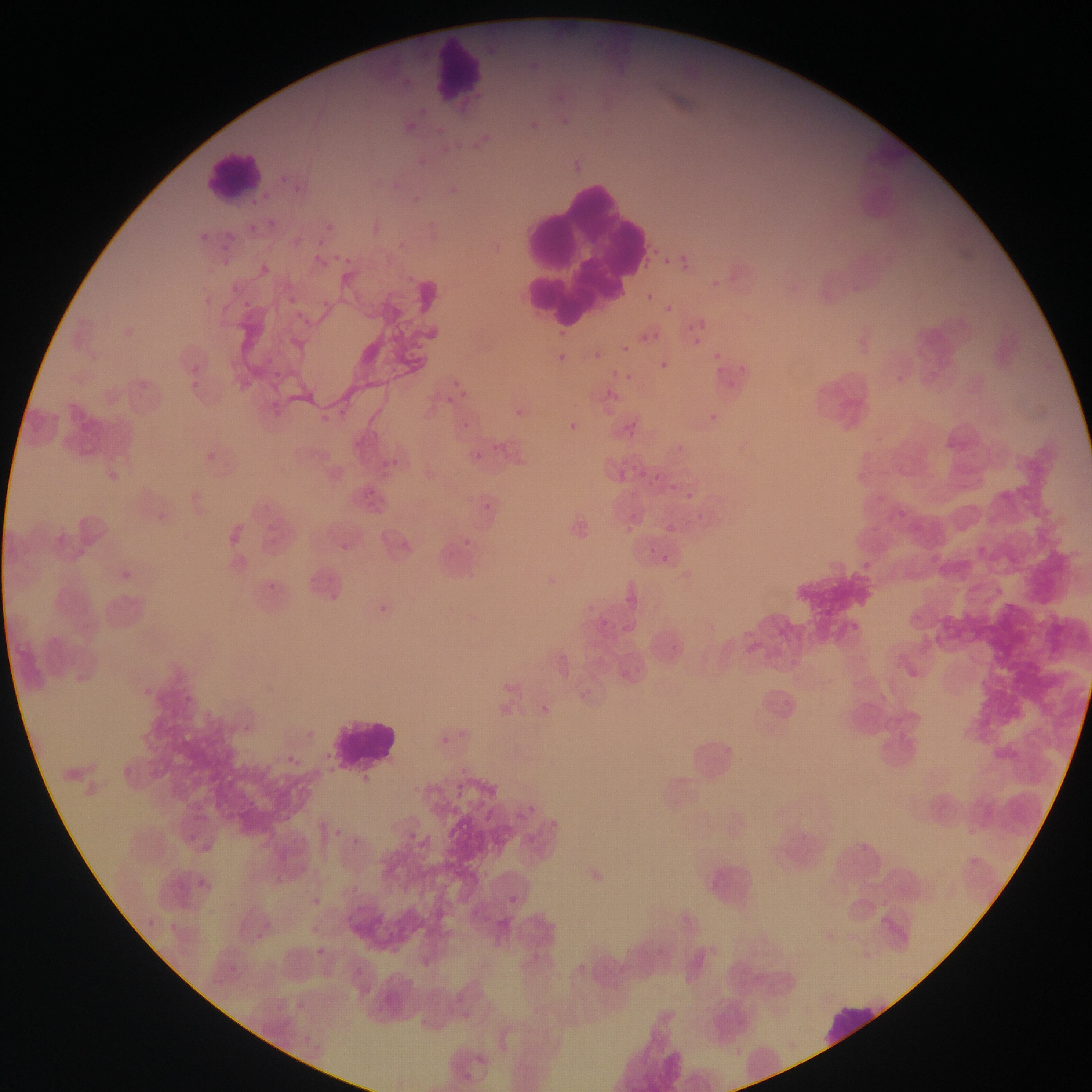

Approximate bounding boxes as left top right bottom in pixels. Plasmodium parasite locations: 481 48 502 57; 533 56 541 66; 402 113 417 127; 562 115 580 135; 524 123 536 135; 466 134 490 156; 288 167 306 192; 407 189 424 207; 254 207 290 226; 316 209 336 230; 219 230 237 255; 311 236 330 254; 318 241 339 269; 662 257 670 265; 254 263 269 281; 646 293 655 302; 665 305 674 314; 687 323 696 333; 653 332 662 341; 558 333 571 341; 622 345 630 354; 590 347 608 361; 554 355 564 363; 707 357 728 379; 659 361 669 370; 623 365 635 378; 273 371 281 378; 190 375 204 393; 445 382 463 406; 566 414 581 437; 707 414 715 427; 460 417 474 430; 203 449 225 470; 616 450 637 468; 474 451 482 460; 651 459 671 488; 110 464 122 482; 897 468 906 477; 682 485 709 507; 484 502 492 511; 899 510 907 519; 666 524 676 533; 625 526 633 534; 462 538 472 550; 341 543 350 551; 977 546 985 555; 661 554 669 562; 103 570 128 595; 375 596 391 611; 540 692 560 718; 177 696 203 722; 441 724 456 752; 451 780 466 800; 514 807 535 825; 331 830 342 843; 354 840 368 854; 191 872 205 894; 312 886 323 906; 508 894 518 905; 311 927 319 935; 316 947 325 956 | approximate x y pixel centers of objects too small to bound: 866 565. Leukocyte locations: 402 36 485 90; 201 149 265 206; 519 163 645 329; 327 718 397 771; 821 1001 892 1045. Collected in Ghana. Photographed through a microscope with a mobile-phone camera. Image is 1092×1092 pixels. One field of view. Thin blood smear.